Report the malaria status of this cell.
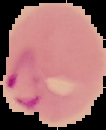
It is parasitized.

Summary:
  - Image type: segmented cell region on a black background
  - Image size: 106×130 pixels
  - Preparation: thin blood film